Assess this cell for malaria.
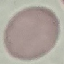

Uninfected.

Thin blood film. Cell patch, automatically extracted from a larger field of view and resized to 64 × 64 pixels. Photographed with a smartphone camera at the microscope eyepiece. Giemsa-stained preparation.